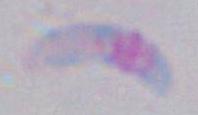
modality = micrograph
identification = Toxoplasma gondii
magnification = 1000x